Classify this cell by malaria status.
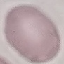

It is uninfected.

stain = Giemsa
image type = automatically extracted cell patch, resized to 64 × 64 pixels
capture = smartphone camera at the microscope eyepiece
preparation = thin smear